State the blood parasite species.
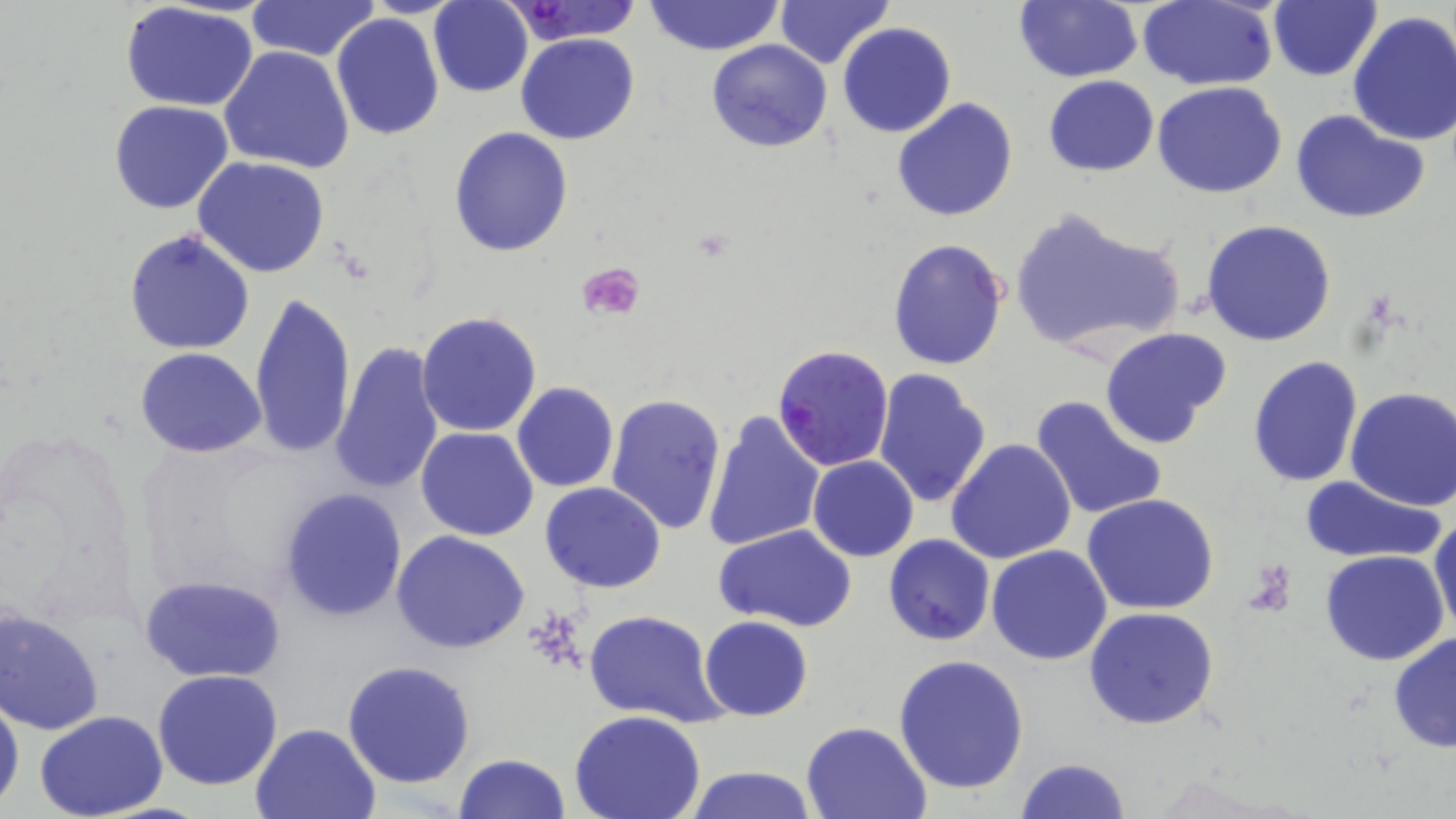

Plasmodium falciparum.

Summary:
  - Coordinate format: approximate bounding boxes as named x1/y1/x2/y2 corners in pixels
  - Uninfected red blood cell locations: (x1=504, y1=0, x2=643, y2=44), (x1=645, y1=0, x2=784, y2=55), (x1=774, y1=0, x2=893, y2=68), (x1=1013, y1=0, x2=1141, y2=83), (x1=1139, y1=0, x2=1279, y2=90), (x1=247, y1=1, x2=379, y2=61), (x1=429, y1=1, x2=533, y2=97), (x1=1267, y1=2, x2=1382, y2=81), (x1=119, y1=3, x2=261, y2=112), (x1=1346, y1=11, x2=1456, y2=148), (x1=331, y1=14, x2=444, y2=140), (x1=837, y1=22, x2=955, y2=138), (x1=229, y1=26, x2=439, y2=155), (x1=515, y1=32, x2=639, y2=145), (x1=706, y1=39, x2=832, y2=154), (x1=220, y1=46, x2=354, y2=174), (x1=1043, y1=75, x2=1159, y2=176), (x1=478, y1=77, x2=602, y2=227), (x1=1153, y1=82, x2=1287, y2=199), (x1=892, y1=98, x2=1019, y2=223), (x1=109, y1=100, x2=234, y2=215), (x1=1291, y1=110, x2=1430, y2=224), (x1=448, y1=127, x2=574, y2=256), (x1=192, y1=156, x2=332, y2=278), (x1=1008, y1=205, x2=1184, y2=358), (x1=1200, y1=220, x2=1337, y2=346), (x1=123, y1=228, x2=256, y2=355), (x1=887, y1=237, x2=1009, y2=371), (x1=249, y1=289, x2=356, y2=458), (x1=416, y1=311, x2=543, y2=436), (x1=1099, y1=326, x2=1231, y2=449), (x1=331, y1=343, x2=444, y2=495), (x1=137, y1=348, x2=267, y2=457), (x1=1247, y1=355, x2=1363, y2=488), (x1=873, y1=367, x2=993, y2=509), (x1=511, y1=381, x2=620, y2=492), (x1=1346, y1=387, x2=1456, y2=511), (x1=604, y1=392, x2=727, y2=535), (x1=1029, y1=394, x2=1167, y2=525), (x1=702, y1=409, x2=825, y2=552), (x1=415, y1=425, x2=540, y2=541), (x1=946, y1=439, x2=1077, y2=566), (x1=808, y1=455, x2=919, y2=562), (x1=1298, y1=474, x2=1446, y2=564), (x1=540, y1=481, x2=666, y2=595), (x1=279, y1=488, x2=408, y2=620), (x1=1081, y1=494, x2=1219, y2=614), (x1=1430, y1=513, x2=1456, y2=636), (x1=714, y1=524, x2=857, y2=633), (x1=391, y1=529, x2=530, y2=654), (x1=884, y1=535, x2=994, y2=645), (x1=987, y1=545, x2=1113, y2=665), (x1=1319, y1=549, x2=1449, y2=666), (x1=139, y1=574, x2=286, y2=681), (x1=1, y1=605, x2=104, y2=735), (x1=1084, y1=606, x2=1218, y2=731), (x1=582, y1=610, x2=725, y2=728), (x1=701, y1=616, x2=813, y2=721), (x1=1388, y1=631, x2=1456, y2=753), (x1=894, y1=654, x2=1028, y2=794), (x1=341, y1=660, x2=476, y2=788), (x1=152, y1=669, x2=283, y2=791), (x1=0, y1=691, x2=23, y2=810), (x1=33, y1=711, x2=168, y2=819), (x1=570, y1=711, x2=707, y2=819), (x1=801, y1=720, x2=931, y2=818), (x1=251, y1=721, x2=380, y2=818), (x1=453, y1=753, x2=571, y2=819), (x1=1013, y1=757, x2=1130, y2=819), (x1=680, y1=765, x2=820, y2=819)
  - Platelet locations: (x1=577, y1=262, x2=646, y2=321)
  - Plasmodium falciparum-infected red blood cell locations: (x1=770, y1=342, x2=894, y2=470)
  - Image size: 1456×819 pixels
  - Stain: May-Grünwald-Giemsa
  - Modality: optical microscopy
  - Field of view: one of a larger specimen
  - Preparation: thin blood smear
  - Magnification: 1000x